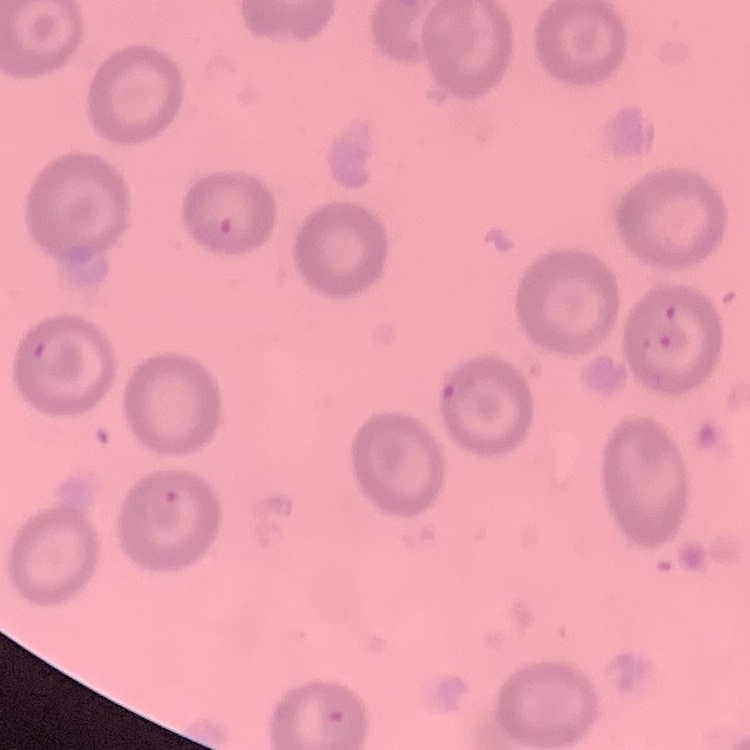

The red blood cells exhibit no rouleaux formation. Field's or Giemsa stain. Thin peripheral smear. Square crop of a larger photomicrograph.